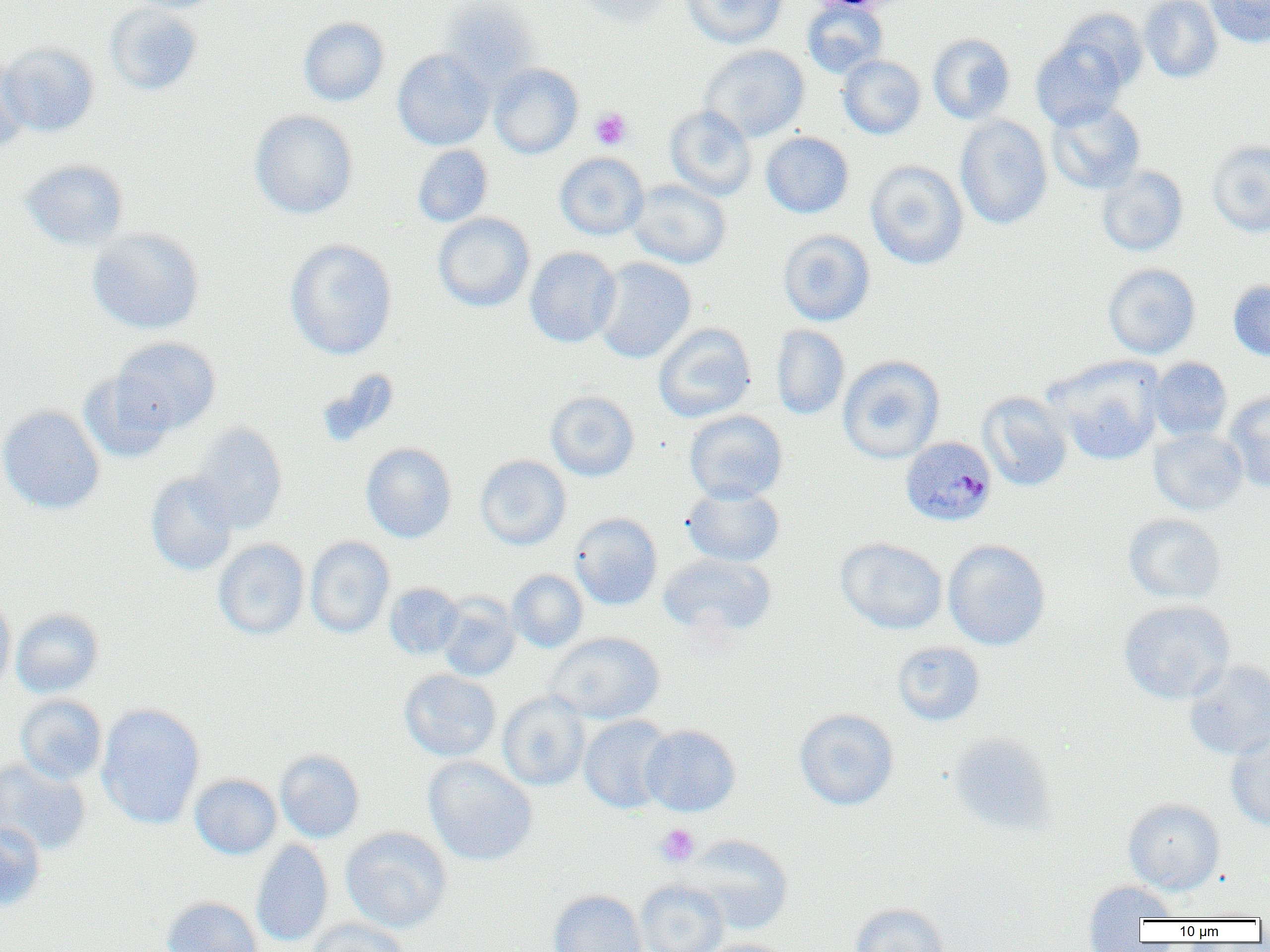
slide-level diagnosis = Plasmodium malariae
image size = 1270×952 pixels
magnification = 1000x
field of view = single
uninfected red blood cell locations = approximate bounding boxes as (x1, y1, x2, y2) in pixels: (125, 0, 223, 13), (575, 0, 674, 27), (681, 0, 788, 48), (1139, 0, 1223, 83), (1205, 0, 1270, 48), (442, 1, 541, 89), (802, 1, 888, 79), (105, 4, 203, 96), (1056, 8, 1149, 93), (298, 17, 390, 106), (928, 33, 1015, 124), (1031, 37, 1128, 130), (0, 42, 100, 137), (700, 45, 809, 142), (392, 49, 494, 150), (0, 55, 31, 150), (837, 55, 926, 140), (489, 63, 583, 159), (1046, 99, 1146, 194), (665, 105, 756, 201), (249, 110, 358, 220), (955, 114, 1053, 230), (761, 132, 854, 218), (1207, 140, 1270, 237), (412, 145, 493, 227), (554, 152, 649, 240), (20, 159, 129, 251), (865, 160, 968, 270), (1096, 166, 1188, 256), (628, 179, 731, 269), (433, 212, 535, 312), (87, 228, 205, 335), (778, 229, 875, 326), (284, 239, 398, 360), (525, 247, 621, 348), (594, 257, 696, 364), (1103, 263, 1201, 358), (1228, 279, 1270, 362), (653, 322, 756, 423), (771, 324, 849, 420), (111, 336, 221, 435), (837, 355, 945, 464), (1047, 356, 1165, 466), (1148, 357, 1232, 442), (79, 371, 174, 463), (545, 390, 639, 481), (977, 391, 1073, 491), (1223, 391, 1270, 492), (0, 405, 105, 514), (685, 409, 787, 504), (191, 423, 288, 533), (1149, 428, 1248, 516), (360, 442, 457, 543), (475, 454, 571, 550), (146, 471, 239, 576), (683, 484, 785, 567), (569, 512, 663, 610), (1123, 513, 1227, 604), (305, 536, 395, 638), (836, 538, 947, 634), (212, 539, 309, 640), (943, 539, 1051, 651), (658, 553, 777, 639), (507, 569, 588, 653), (384, 583, 464, 660), (0, 593, 16, 695), (437, 593, 520, 681), (1118, 600, 1235, 705), (11, 608, 104, 698), (545, 631, 665, 725), (892, 641, 985, 725), (1184, 661, 1270, 759), (399, 669, 501, 762), (497, 692, 591, 791), (15, 694, 107, 785), (96, 702, 205, 829), (794, 708, 898, 811), (578, 714, 674, 814), (641, 724, 741, 816), (1226, 731, 1270, 831), (947, 732, 1057, 835), (274, 749, 365, 843), (423, 756, 537, 866), (0, 758, 91, 856), (189, 764, 365, 848), (189, 774, 281, 859), (1123, 798, 1225, 894), (0, 822, 46, 911), (340, 826, 452, 933), (683, 834, 794, 934), (251, 839, 334, 947), (635, 879, 729, 952), (1083, 879, 1180, 932), (547, 890, 647, 952), (161, 896, 262, 952), (849, 902, 951, 952), (307, 920, 408, 951), (699, 938, 796, 952)
platelet locations = approximate bounding boxes as (x1, y1, x2, y2) in pixels: (590, 107, 632, 149), (655, 824, 699, 867)
modality = light microscopy
Plasmodium malariae-infected red blood cell locations = approximate bounding boxes as (x1, y1, x2, y2) in pixels: (901, 436, 997, 527)
preparation = thin blood smear